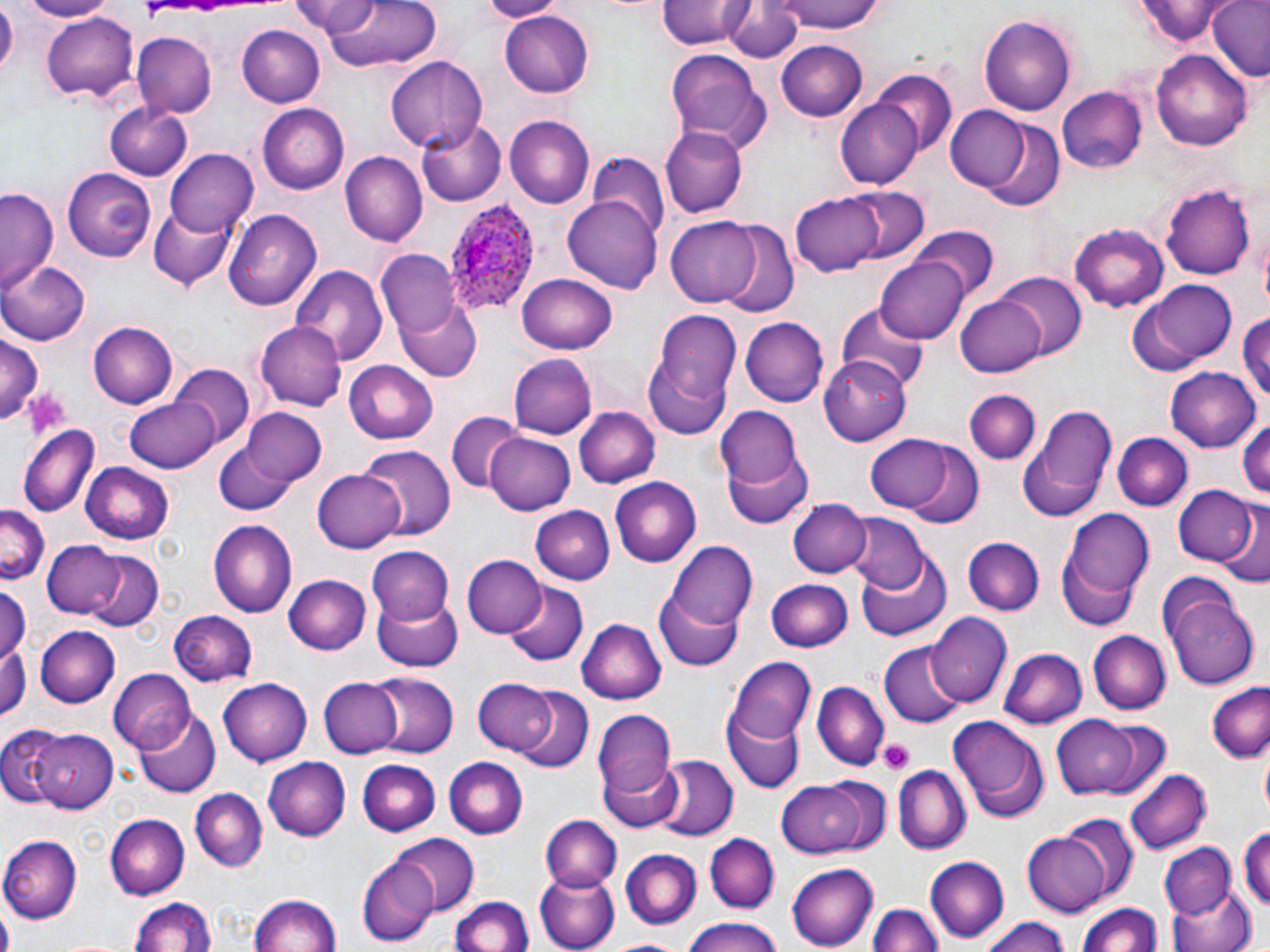
slide_level_diagnosis: Plasmodium ovale
uninfected_red_blood_cell_locations: 'approximate bounding boxes as (x1, y1, x2, y2) in pixels: (0, 0, 18, 82), (16, 0, 118, 22), (289, 0, 388, 37), (478, 0, 560, 21), (655, 0, 752, 51), (764, 0, 891, 35), (1131, 1, 1236, 44), (1207, 1, 1269, 82), (315, 2, 444, 71), (725, 2, 806, 63), (39, 10, 139, 105), (500, 10, 595, 98), (979, 16, 1077, 115), (236, 23, 326, 108), (131, 33, 216, 116), (775, 39, 868, 121), (1152, 48, 1253, 148), (664, 50, 772, 153), (387, 57, 487, 153), (871, 70, 956, 159), (1057, 88, 1148, 172), (835, 97, 924, 190), (105, 101, 194, 180), (259, 104, 352, 194), (944, 106, 1035, 192), (505, 117, 593, 208), (417, 122, 505, 205), (979, 122, 1065, 212), (661, 125, 747, 217), (165, 149, 259, 239), (343, 152, 428, 245), (588, 155, 669, 243), (63, 169, 156, 260), (1162, 182, 1255, 281), (834, 186, 931, 268), (1, 187, 61, 295), (791, 192, 886, 275), (564, 194, 662, 294), (148, 202, 235, 288), (227, 210, 321, 310), (667, 216, 766, 306), (712, 220, 801, 318), (1069, 225, 1166, 312), (912, 228, 1000, 303), (378, 248, 462, 336), (876, 255, 970, 343), (2, 261, 89, 345), (292, 265, 387, 366), (993, 272, 1086, 361), (517, 273, 618, 354), (1137, 280, 1236, 369), (956, 292, 1051, 380), (395, 296, 482, 382), (835, 299, 931, 394), (654, 311, 742, 408), (1236, 312, 1270, 411), (740, 317, 830, 408), (88, 320, 178, 408), (254, 323, 346, 411), (0, 334, 41, 427), (642, 344, 735, 438), (820, 353, 909, 446), (508, 354, 595, 439), (343, 360, 440, 443), (169, 365, 256, 451), (1166, 366, 1260, 452), (965, 389, 1039, 464), (125, 396, 222, 472), (1018, 404, 1116, 521), (235, 407, 327, 493), (716, 407, 810, 521), (575, 409, 659, 489), (447, 412, 526, 494), (1235, 417, 1270, 501), (19, 423, 99, 513), (208, 425, 313, 517), (485, 431, 575, 514), (866, 432, 959, 513), (1112, 433, 1191, 511), (899, 442, 985, 530), (358, 443, 456, 539), (81, 462, 173, 544), (313, 468, 406, 553), (610, 477, 701, 566), (1172, 485, 1257, 566), (786, 499, 870, 577), (1216, 499, 1269, 587), (0, 505, 49, 584), (532, 506, 615, 586), (1059, 509, 1155, 623), (842, 513, 929, 594), (207, 519, 297, 616), (963, 538, 1043, 614), (43, 541, 126, 619), (667, 543, 756, 629), (365, 544, 454, 623), (83, 552, 162, 632), (856, 554, 953, 642), (464, 555, 544, 638), (283, 574, 370, 655), (766, 579, 853, 653), (502, 581, 586, 667), (0, 583, 28, 661), (653, 586, 746, 671), (372, 593, 463, 672), (1167, 593, 1260, 689), (169, 609, 258, 688), (928, 612, 1009, 708), (578, 617, 665, 706), (36, 626, 119, 707), (1090, 630, 1169, 715), (0, 642, 29, 721), (879, 644, 964, 727), (999, 647, 1088, 728), (726, 658, 814, 746), (108, 669, 194, 754), (366, 673, 459, 756), (218, 677, 312, 766), (319, 677, 403, 759), (472, 679, 560, 757), (811, 681, 890, 770), (1208, 682, 1270, 763), (506, 687, 593, 772), (136, 709, 218, 798), (594, 711, 675, 798), (723, 712, 804, 793), (946, 714, 1050, 822), (1053, 716, 1141, 799), (1092, 717, 1174, 800), (1, 727, 69, 807), (31, 728, 117, 811), (651, 754, 737, 841), (444, 757, 528, 838), (264, 759, 351, 840), (600, 760, 685, 833), (358, 761, 442, 835), (892, 765, 969, 854), (1121, 766, 1213, 855), (779, 777, 875, 857), (190, 788, 267, 872), (105, 814, 189, 899), (1060, 815, 1139, 904), (540, 816, 621, 891), (1238, 827, 1270, 914), (1023, 833, 1115, 914), (394, 834, 478, 915), (704, 834, 778, 913), (0, 836, 80, 923), (1159, 843, 1238, 921), (618, 848, 701, 930), (358, 854, 439, 944), (924, 857, 1007, 943), (700, 864, 779, 946), (786, 864, 878, 949), (534, 869, 619, 951), (815, 880, 937, 952), (1170, 882, 1257, 952), (247, 892, 343, 952), (133, 896, 217, 952), (454, 896, 533, 952), (1077, 901, 1165, 952), (867, 903, 942, 952), (680, 916, 785, 952), (981, 916, 1072, 952), (602, 937, 695, 952)'
modality: optical microscopy
platelet_locations: 'approximate bounding boxes as (x1, y1, x2, y2) in pixels: (24, 388, 72, 435), (878, 738, 915, 774)'
field_of_view: single
magnification: 1000x
preparation: thin blood film
image_size: 1270×952 pixels
stain: May-Grünwald-Giemsa
plasmodium_ovale_infected_red_blood_cell_locations: 'approximate bounding boxes as (x1, y1, x2, y2) in pixels: (445, 203, 544, 326)'